Identify the blood parasite species.
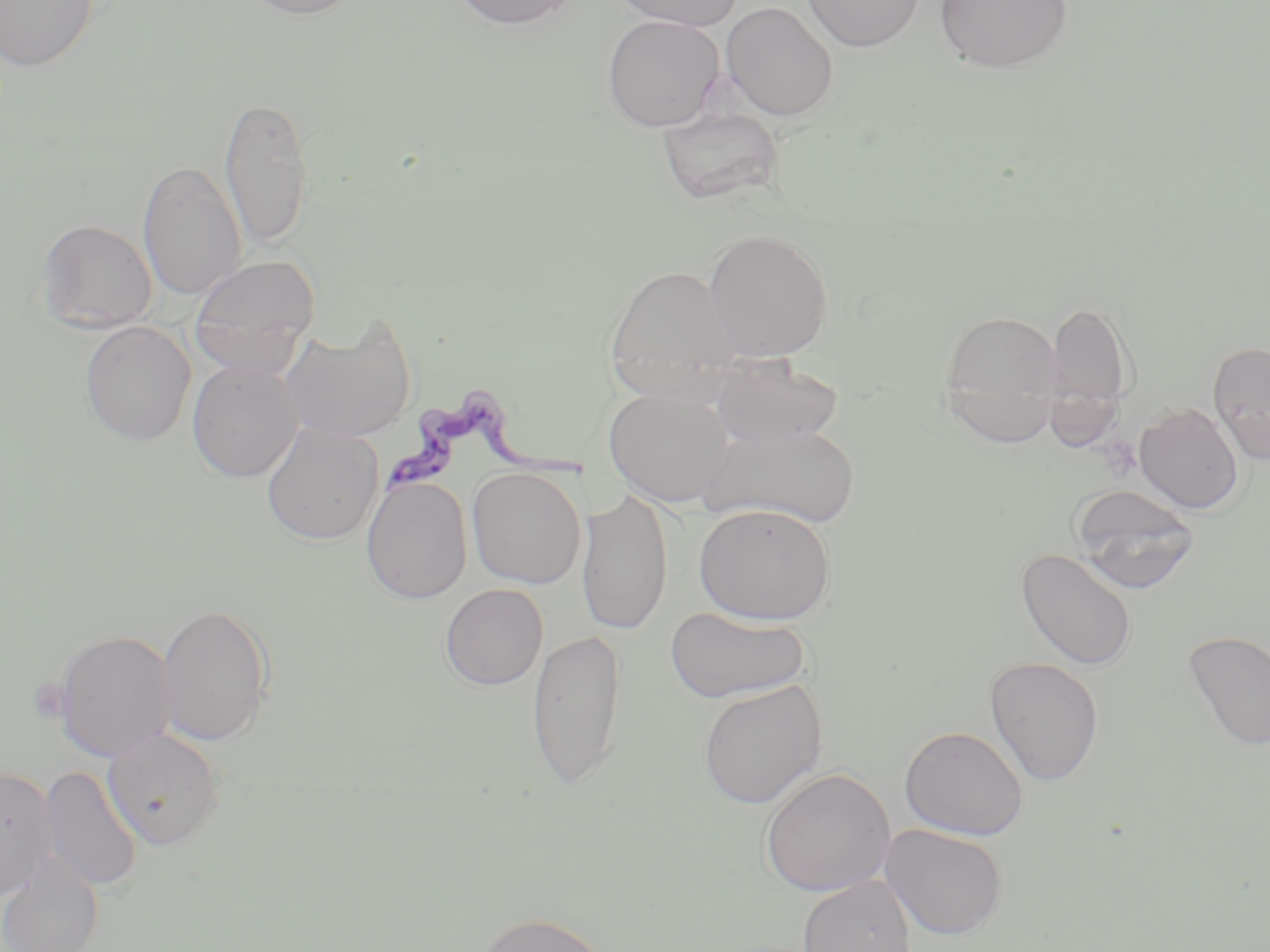

Trypanosoma brucei.

Approximate bounding boxes as named x1/y1/x2/y2 corners in pixels. Uninfected red blood cell locations: (x1=0, y1=0, x2=98, y2=72), (x1=241, y1=0, x2=366, y2=20), (x1=450, y1=0, x2=579, y2=30), (x1=614, y1=0, x2=744, y2=30), (x1=802, y1=0, x2=924, y2=51), (x1=934, y1=0, x2=1074, y2=74), (x1=721, y1=1, x2=838, y2=121), (x1=602, y1=14, x2=724, y2=132), (x1=218, y1=93, x2=315, y2=248), (x1=657, y1=107, x2=783, y2=205), (x1=138, y1=160, x2=246, y2=301), (x1=36, y1=219, x2=157, y2=333), (x1=703, y1=228, x2=834, y2=362), (x1=190, y1=253, x2=320, y2=375), (x1=603, y1=263, x2=742, y2=403), (x1=1046, y1=299, x2=1137, y2=418), (x1=939, y1=308, x2=1065, y2=446), (x1=282, y1=319, x2=417, y2=443), (x1=80, y1=321, x2=196, y2=446), (x1=1207, y1=341, x2=1270, y2=464), (x1=708, y1=354, x2=843, y2=451), (x1=187, y1=360, x2=304, y2=483), (x1=604, y1=387, x2=737, y2=507), (x1=1134, y1=402, x2=1244, y2=514), (x1=262, y1=422, x2=384, y2=545), (x1=699, y1=422, x2=861, y2=529), (x1=467, y1=467, x2=586, y2=588), (x1=361, y1=475, x2=472, y2=604), (x1=1068, y1=484, x2=1200, y2=594), (x1=576, y1=489, x2=674, y2=636), (x1=694, y1=503, x2=837, y2=625), (x1=1015, y1=547, x2=1138, y2=672), (x1=440, y1=583, x2=548, y2=691), (x1=157, y1=602, x2=274, y2=746), (x1=665, y1=606, x2=810, y2=704), (x1=527, y1=626, x2=627, y2=790), (x1=52, y1=629, x2=178, y2=761), (x1=1182, y1=629, x2=1270, y2=753), (x1=984, y1=657, x2=1104, y2=788), (x1=697, y1=680, x2=826, y2=809), (x1=899, y1=725, x2=1029, y2=840), (x1=103, y1=727, x2=225, y2=850), (x1=41, y1=765, x2=142, y2=893), (x1=0, y1=766, x2=59, y2=897), (x1=760, y1=766, x2=895, y2=897), (x1=880, y1=823, x2=1010, y2=940), (x1=0, y1=854, x2=104, y2=952), (x1=797, y1=875, x2=917, y2=952), (x1=474, y1=911, x2=615, y2=952). Trypanosoma brucei locations: (x1=383, y1=391, x2=597, y2=496). Thin blood smear. One field of a larger specimen. 1000x magnification. Image is 1270×952 pixels. May-Grünwald-Giemsa-stained preparation. Light microscopy.